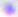

identification = Toxoplasma gondii
magnification = 400x
modality = photomicrograph